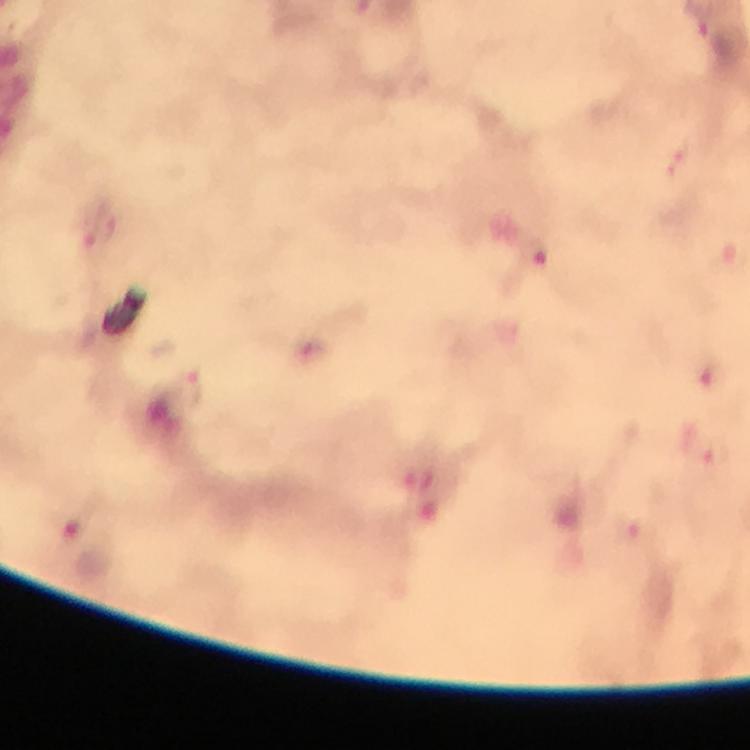 Approximate centers as {x, y} in pixels. Plasmodium parasite locations: {678, 160}, {102, 226}, {535, 254}, {708, 371}, {188, 388}, {717, 452}, {637, 533}. 100x magnification. Giemsa-stained preparation. Smartphone photograph taken through a microscope. Image is 750×750 pixels. Immersion oil was used. Thick smear. From a diagnostic examination for malaria. A crop from one field of view.